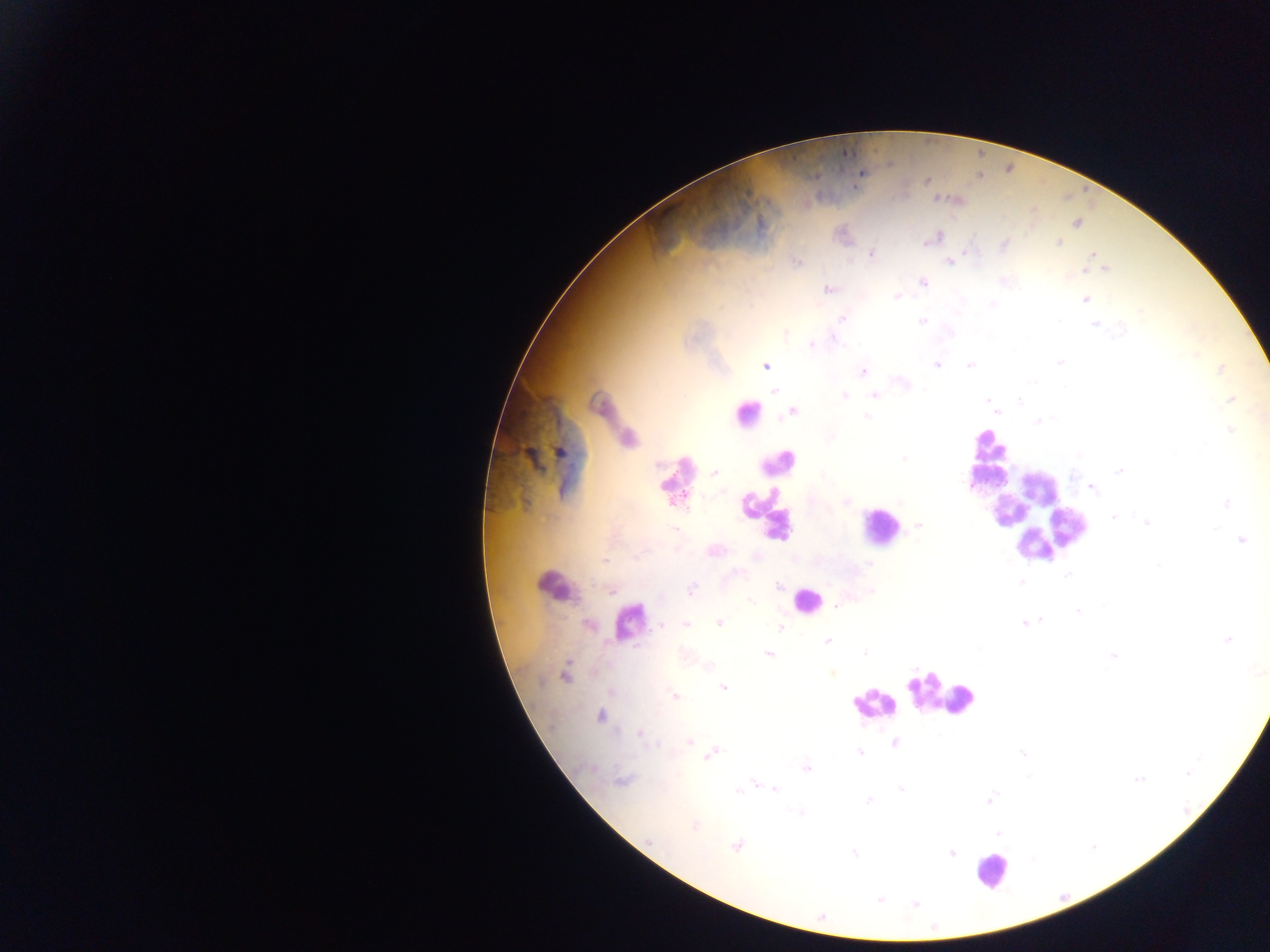
{
  "image_size": "1270×952 pixels",
  "field_of_view": "single",
  "malaria_parasite_locations": "approximate centers as [x, y] in pixels: [927, 181], [1076, 224], [933, 238], [1059, 243], [1004, 245], [871, 254], [1091, 254], [950, 261], [798, 262], [1106, 268], [924, 283], [828, 289], [897, 296], [1085, 300], [992, 304], [843, 318], [922, 320], [1095, 325], [786, 334], [833, 339], [812, 345], [1059, 362], [937, 365], [765, 366], [969, 366], [1221, 369], [863, 371], [904, 384], [774, 390], [845, 396], [875, 396], [1230, 399], [988, 401], [1020, 401], [792, 412], [867, 416], [1037, 421], [1230, 430], [560, 452], [904, 459], [1119, 471], [714, 473], [1092, 487], [1226, 502], [1113, 517], [1146, 523], [919, 525], [1241, 540], [715, 551], [1158, 564], [870, 565], [1067, 575], [1021, 582], [779, 586], [691, 590], [751, 602], [837, 605], [1078, 611], [1040, 620], [1025, 622], [719, 623], [661, 625], [686, 625], [781, 627], [827, 640], [1227, 640], [865, 652], [768, 654], [1113, 656], [565, 675], [723, 687], [675, 696], [601, 716], [640, 733], [689, 742], [895, 744], [860, 752], [1022, 752], [712, 754], [807, 768], [1187, 774], [622, 780], [1139, 780], [756, 784], [749, 787], [775, 789], [901, 790], [740, 791], [990, 799], [868, 801], [800, 813], [694, 825], [998, 833], [650, 841], [736, 846], [951, 853], [854, 854], [880, 899], [915, 903]",
  "country": "Ghana",
  "preparation": "thick blood smear",
  "leukocyte_locations": "approximate centers as [x, y] in pixels: [746, 411], [615, 424], [987, 455], [777, 461], [671, 478], [1037, 512], [1005, 513], [765, 514], [876, 528], [558, 581], [805, 599], [628, 621], [942, 700], [873, 704], [992, 870]",
  "capture": "mobile-phone photograph through a microscope"
}